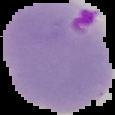
{
  "image_size": "115×115 pixels",
  "preparation": "thin blood smear",
  "result": "malaria parasites identified",
  "image_type": "segmented cell region with the area outside set to black"
}